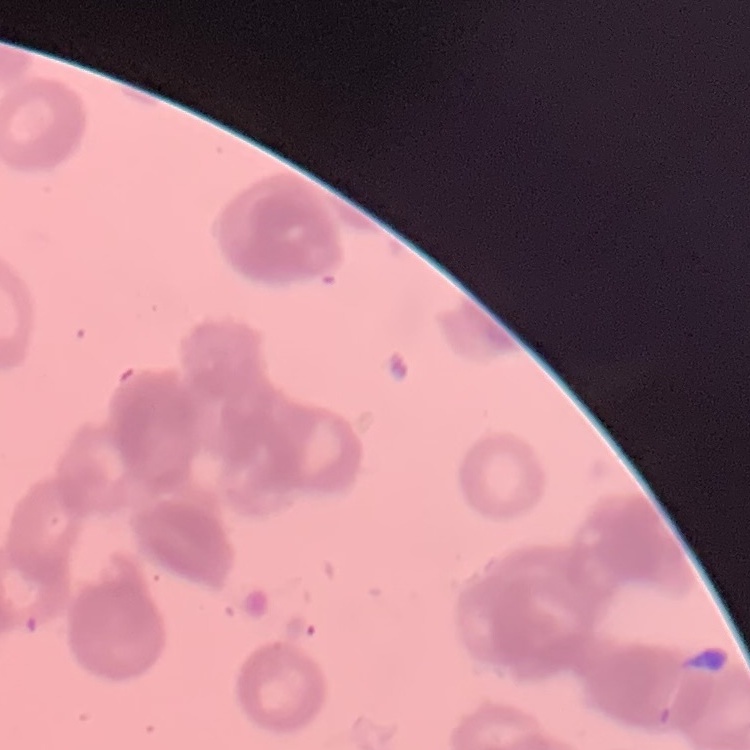
The red blood cells exhibit rouleaux formation. Thin peripheral smear. Stained with either Field's or Giemsa. Square crop of a larger photomicrograph.